Comment on the morphology of the red blood cells.
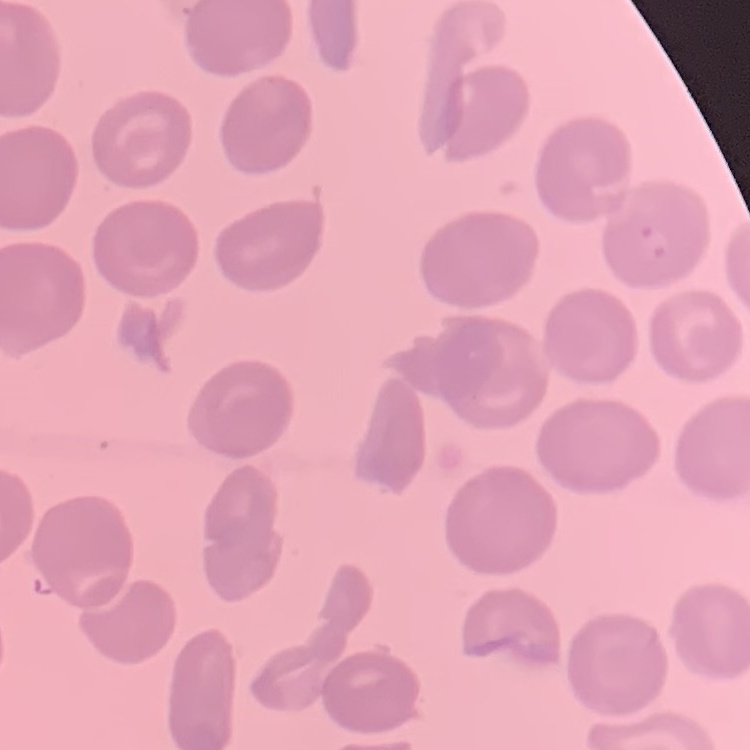
No rouleaux formation.

Summary:
  - Preparation: thin blood film
  - Stain: Field's or Giemsa
  - Image type: one tile cut from a larger photomicrograph